Locate every Trypanosoma brucei.
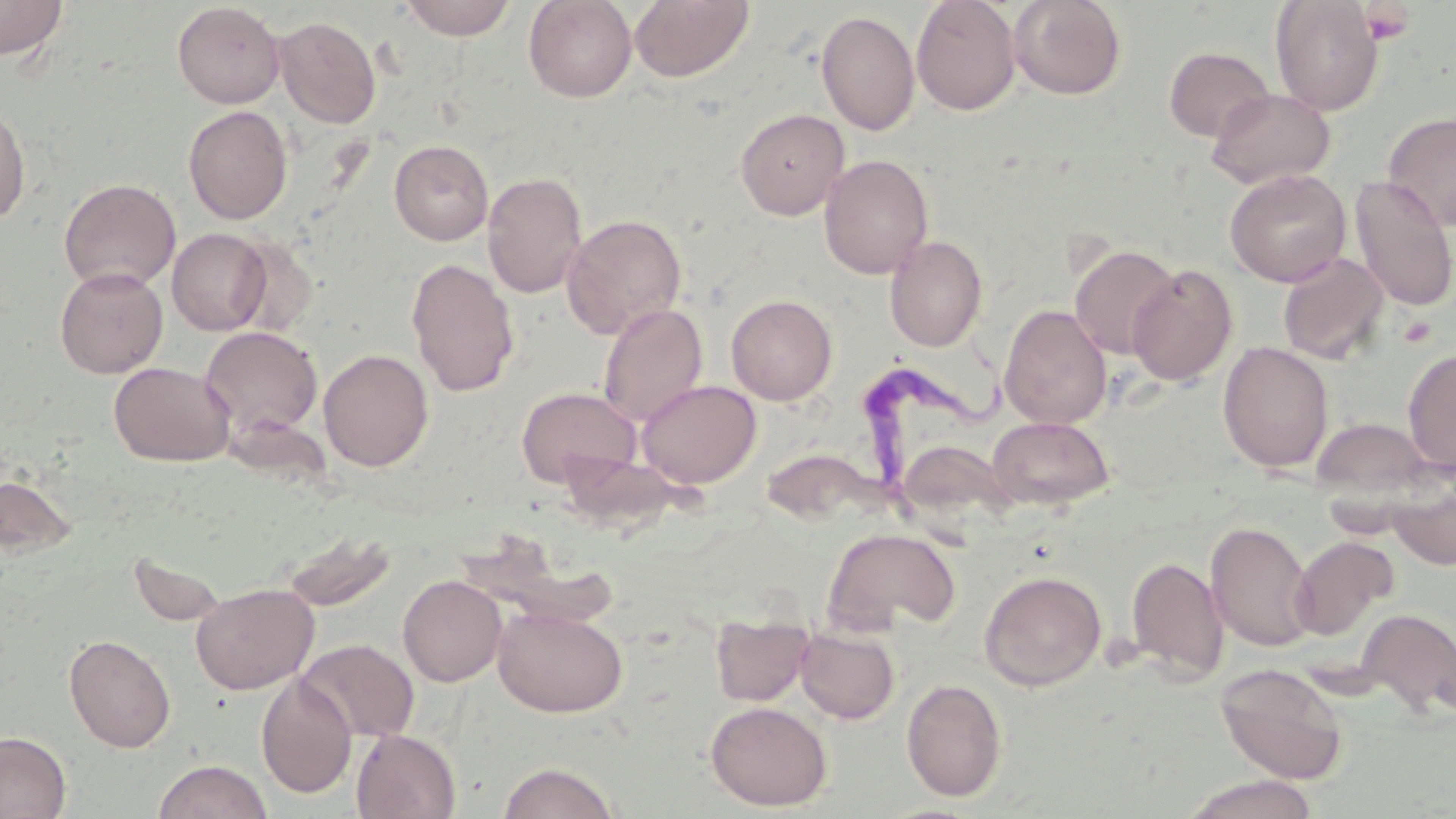
Approximate bounding boxes as named x1/y1/x2/y2 corners in pixels.
Trypanosoma brucei: (x1=859, y1=345, x2=1011, y2=498).

slide-level diagnosis = Trypanosoma brucei
platelet locations = approximate bounding boxes as named x1/y1/x2/y2 corners in pixels: (x1=1362, y1=4, x2=1413, y2=45), (x1=1397, y1=317, x2=1437, y2=348)
stain = May-Grünwald-Giemsa
modality = light microscopy
uninfected red blood cell locations = approximate bounding boxes as named x1/y1/x2/y2 corners in pixels: (x1=398, y1=0, x2=518, y2=40), (x1=523, y1=0, x2=637, y2=103), (x1=629, y1=0, x2=755, y2=83), (x1=911, y1=0, x2=1021, y2=116), (x1=1008, y1=0, x2=1127, y2=100), (x1=1271, y1=0, x2=1383, y2=115), (x1=0, y1=1, x2=68, y2=60), (x1=172, y1=2, x2=285, y2=108), (x1=816, y1=10, x2=920, y2=136), (x1=274, y1=16, x2=381, y2=128), (x1=1163, y1=46, x2=1274, y2=142), (x1=1206, y1=87, x2=1335, y2=190), (x1=0, y1=102, x2=31, y2=225), (x1=183, y1=105, x2=293, y2=225), (x1=735, y1=108, x2=850, y2=220), (x1=1383, y1=112, x2=1456, y2=230), (x1=389, y1=139, x2=494, y2=245), (x1=819, y1=154, x2=933, y2=279), (x1=1225, y1=168, x2=1351, y2=287), (x1=482, y1=171, x2=587, y2=298), (x1=1351, y1=177, x2=1456, y2=311), (x1=59, y1=178, x2=180, y2=292), (x1=561, y1=214, x2=687, y2=339), (x1=167, y1=228, x2=271, y2=335), (x1=885, y1=234, x2=987, y2=352), (x1=1070, y1=244, x2=1179, y2=360), (x1=1278, y1=253, x2=1389, y2=364), (x1=406, y1=258, x2=520, y2=397), (x1=1127, y1=264, x2=1238, y2=386), (x1=54, y1=266, x2=168, y2=378), (x1=726, y1=294, x2=837, y2=405), (x1=597, y1=303, x2=708, y2=427), (x1=998, y1=304, x2=1112, y2=429), (x1=199, y1=326, x2=323, y2=441), (x1=1218, y1=341, x2=1334, y2=473), (x1=1403, y1=348, x2=1456, y2=472), (x1=318, y1=349, x2=433, y2=472), (x1=108, y1=361, x2=236, y2=466), (x1=637, y1=380, x2=761, y2=488), (x1=516, y1=386, x2=642, y2=489), (x1=987, y1=416, x2=1115, y2=510), (x1=1312, y1=416, x2=1439, y2=507), (x1=895, y1=439, x2=1018, y2=529), (x1=554, y1=450, x2=691, y2=530), (x1=1385, y1=464, x2=1456, y2=571), (x1=0, y1=474, x2=77, y2=558), (x1=1206, y1=520, x2=1315, y2=653), (x1=822, y1=528, x2=960, y2=634), (x1=279, y1=532, x2=398, y2=611), (x1=1291, y1=536, x2=1397, y2=640), (x1=1126, y1=556, x2=1228, y2=682), (x1=979, y1=570, x2=1106, y2=691), (x1=398, y1=575, x2=506, y2=686), (x1=191, y1=582, x2=319, y2=694), (x1=493, y1=603, x2=628, y2=717), (x1=1357, y1=609, x2=1456, y2=719), (x1=710, y1=614, x2=813, y2=706), (x1=795, y1=626, x2=900, y2=724), (x1=64, y1=634, x2=176, y2=752), (x1=297, y1=639, x2=419, y2=743), (x1=1215, y1=662, x2=1348, y2=785), (x1=256, y1=673, x2=357, y2=799), (x1=901, y1=678, x2=1008, y2=801), (x1=705, y1=700, x2=832, y2=811), (x1=351, y1=729, x2=461, y2=819), (x1=0, y1=731, x2=71, y2=817), (x1=152, y1=758, x2=274, y2=819), (x1=497, y1=761, x2=622, y2=819), (x1=1179, y1=774, x2=1321, y2=819)
field of view = single
magnification = 1000x
image size = 1456×819 pixels
preparation = thin blood film